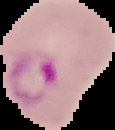
result: Plasmodium parasites identified
image_size: 115×130 pixels
image_type: segmented cell region with the area outside set to black
preparation: thin blood smear